Identify the cell.
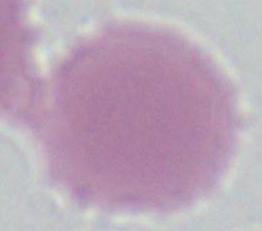
This is an erythrocyte.

modality: micrograph
magnification: 1000x